Report the malaria status of this cell.
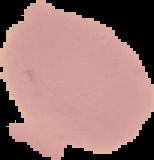
Uninfected.

Image is 154×160 pixels. From a thin blood smear. Cell region segmented out of the field of view; the surrounding area is masked to black.